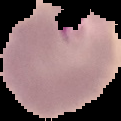

preparation = thin blood smear
image size = 121×121 pixels
image type = segmented cell region with the area outside set to black
malaria status = parasitized